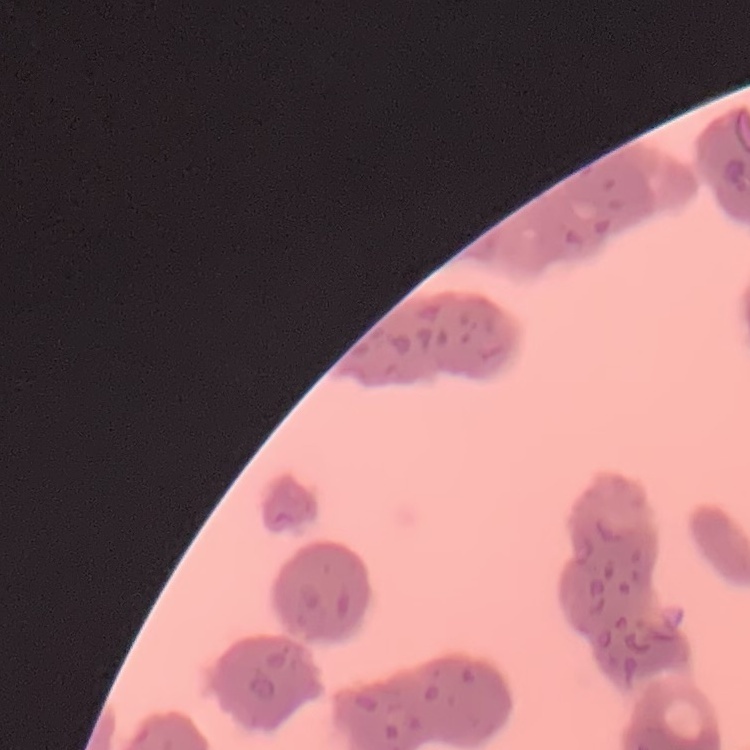
The red blood cells exhibit rouleaux formation. One tile cut from a larger photomicrograph. Field's or Giemsa stain. Thin blood smear.